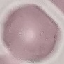
malaria status = uninfected
capture = smartphone through the microscope eyepiece
preparation = thin blood smear
image type = cell patch, automatically extracted from a larger field of view and resized to 64 × 64 pixels
stain = Giemsa